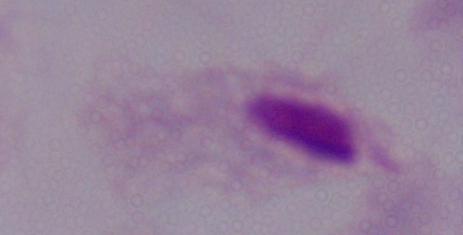

magnification = 1000x
modality = photomicrograph
identification = trichomonad